Identify the cell.
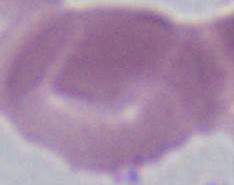

An erythrocyte.

Micrograph. 1000x magnification.